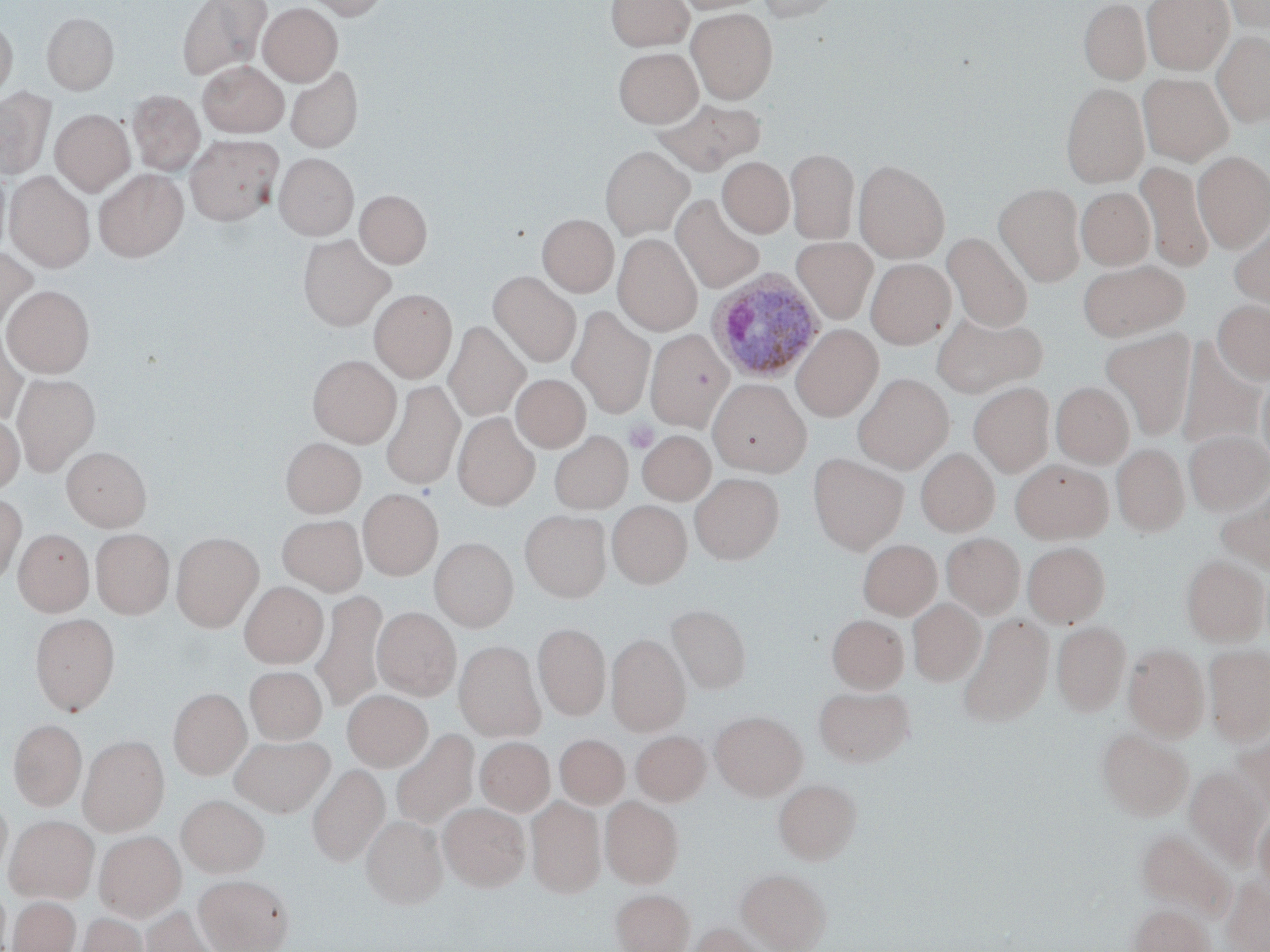

Summary:
  - Coordinate format: approximate bounding boxes as (x1, y1, x2, y2) in pixels
  - Plasmodium ovale-infected red blood cell locations: (706, 270, 826, 384)
  - Uninfected red blood cell locations: (178, 0, 271, 80), (302, 0, 389, 19), (606, 0, 693, 51), (675, 0, 769, 13), (756, 0, 844, 22), (1078, 0, 1151, 85), (1142, 0, 1233, 74), (1221, 0, 1269, 34), (258, 2, 343, 84), (687, 8, 778, 103), (42, 12, 118, 94), (0, 18, 17, 101), (1212, 32, 1270, 127), (614, 44, 702, 128), (197, 61, 289, 137), (285, 66, 362, 152), (1138, 73, 1234, 165), (1060, 82, 1149, 187), (0, 88, 55, 180), (127, 90, 205, 175), (653, 97, 765, 175), (50, 109, 134, 195), (185, 134, 282, 225), (600, 146, 693, 238), (786, 147, 859, 244), (1193, 151, 1270, 251), (274, 153, 358, 239), (717, 157, 794, 238), (854, 159, 950, 262), (1136, 161, 1214, 273), (695, 166, 785, 274), (0, 167, 11, 256), (93, 169, 188, 261), (5, 172, 95, 270), (994, 183, 1087, 286), (1076, 186, 1155, 270), (355, 190, 432, 268), (672, 194, 766, 294), (538, 213, 619, 296), (1229, 215, 1270, 312), (614, 233, 703, 335), (943, 233, 1033, 333), (298, 234, 394, 330), (791, 237, 878, 323), (0, 246, 38, 331), (866, 259, 955, 348), (1078, 260, 1189, 341), (489, 271, 581, 367), (2, 285, 94, 376), (370, 290, 456, 382), (1213, 299, 1270, 385), (568, 305, 655, 417), (931, 311, 1047, 398), (444, 321, 529, 422), (792, 324, 883, 421), (646, 329, 734, 430), (1101, 329, 1197, 441), (0, 330, 27, 424), (1176, 339, 1266, 451), (308, 355, 401, 447), (12, 373, 100, 475), (853, 373, 954, 472), (1257, 373, 1270, 468), (511, 374, 590, 452), (708, 379, 811, 475), (382, 380, 464, 490), (969, 382, 1054, 477), (1051, 382, 1134, 468), (0, 412, 24, 495), (453, 412, 540, 510), (549, 430, 633, 514), (637, 430, 715, 505), (1184, 430, 1270, 515), (281, 437, 365, 516), (1112, 443, 1189, 536), (62, 446, 150, 531), (916, 448, 999, 536), (808, 452, 909, 553), (1010, 459, 1113, 543), (691, 473, 783, 563), (1216, 483, 1270, 575), (358, 489, 442, 580), (0, 494, 26, 587), (607, 500, 692, 588), (520, 510, 611, 602), (278, 514, 367, 596), (13, 528, 93, 616), (91, 528, 174, 618), (171, 532, 263, 630), (942, 533, 1025, 619), (431, 537, 517, 631), (858, 539, 942, 620), (1023, 541, 1110, 627), (1181, 555, 1269, 645), (239, 582, 327, 668), (313, 590, 387, 713), (908, 598, 985, 685), (666, 604, 751, 693), (372, 606, 461, 700), (30, 613, 119, 715), (958, 613, 1054, 727), (827, 614, 909, 693), (1052, 621, 1131, 714), (533, 623, 610, 720), (607, 634, 690, 735), (455, 640, 544, 740), (1124, 644, 1210, 740), (1204, 645, 1270, 744), (245, 666, 327, 744), (814, 685, 914, 766), (169, 688, 251, 778), (343, 689, 432, 771), (710, 711, 807, 800), (8, 719, 87, 810), (1097, 728, 1193, 820), (391, 729, 479, 831), (631, 731, 710, 805), (1233, 732, 1270, 819), (555, 733, 629, 808), (229, 734, 335, 817), (79, 735, 168, 835), (475, 737, 555, 816), (308, 763, 389, 866), (1185, 766, 1268, 866), (773, 778, 861, 864), (0, 794, 12, 880), (177, 794, 269, 876), (527, 796, 605, 897), (601, 796, 683, 888), (440, 802, 529, 891), (1253, 808, 1270, 894), (5, 815, 98, 902), (362, 816, 447, 909), (1137, 829, 1234, 919), (94, 831, 185, 921), (737, 868, 830, 952), (194, 874, 294, 952), (1221, 877, 1270, 952), (0, 884, 10, 951), (611, 889, 694, 952), (8, 897, 80, 952), (1129, 904, 1213, 952), (138, 906, 221, 952), (77, 912, 148, 952), (689, 923, 766, 952)
  - Platelet locations: (624, 420, 659, 454)
  - Slide-level diagnosis: Plasmodium ovale
  - Preparation: thin blood smear
  - Stain: May-Grünwald-Giemsa
  - Modality: optical microscopy
  - Field of view: one of a larger specimen
  - Magnification: 1000x
  - Image size: 1270×952 pixels